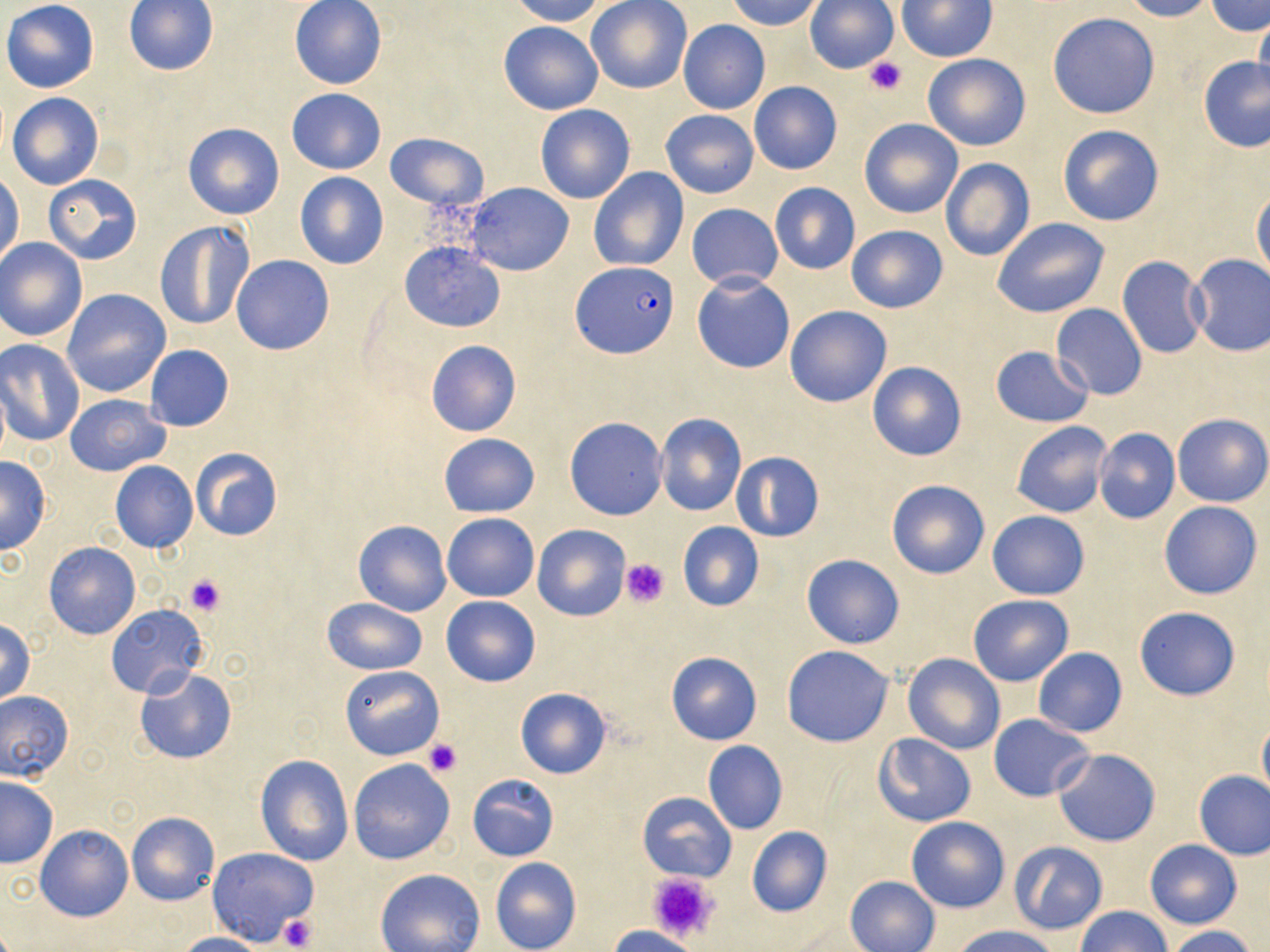

slide_level_diagnosis: Plasmodium falciparum
platelet_locations: 'approximate bounding boxes as (x1,y1)-(x2,y2) corner pairs in pixels: (863,55)-(908,97), (620,558)-(671,608), (184,573)-(227,616), (423,738)-(463,777), (645,871)-(722,947), (276,912)-(318,952)'
field_of_view: one of a larger specimen
preparation: thin blood smear
uninfected_red_blood_cell_locations: 'approximate bounding boxes as (x1,y1)-(x2,y2) corner pairs in pixels: (1,0)-(99,92), (289,0)-(386,89), (506,0)-(605,26), (727,0)-(827,32), (805,0)-(899,74), (1120,0)-(1216,21), (1207,0)-(1270,37), (123,1)-(219,75), (586,1)-(692,94), (897,1)-(996,61), (1047,13)-(1160,119), (1253,13)-(1270,102), (498,19)-(603,115), (678,19)-(770,114), (922,53)-(1031,151), (1197,55)-(1270,152), (749,81)-(842,175), (287,88)-(386,174), (7,92)-(103,190), (535,105)-(635,204), (661,110)-(759,198), (859,118)-(963,218), (183,122)-(284,219), (1057,125)-(1164,227), (384,132)-(486,211), (941,158)-(1034,261), (588,167)-(689,271), (1,169)-(23,268), (295,171)-(389,270), (43,174)-(142,264), (465,182)-(572,275), (770,183)-(860,274), (1251,190)-(1270,285), (687,203)-(782,290), (992,216)-(1111,318), (155,221)-(253,330), (845,225)-(949,312), (0,238)-(87,342), (399,242)-(506,332), (231,254)-(334,355), (1186,254)-(1270,357), (1116,256)-(1209,358), (692,274)-(794,373), (61,289)-(171,398), (1052,304)-(1147,399), (785,305)-(891,407), (0,340)-(85,446), (425,340)-(521,437), (144,344)-(235,432), (989,345)-(1095,427), (866,361)-(967,462), (0,374)-(9,469), (65,393)-(170,476), (655,412)-(747,516), (1174,414)-(1270,507), (565,418)-(667,521), (1011,421)-(1113,518), (1092,428)-(1181,525), (438,433)-(539,517), (189,447)-(284,541), (730,451)-(824,543), (0,454)-(51,556), (110,460)-(198,553), (887,479)-(992,579), (1158,501)-(1263,600), (986,511)-(1089,600), (442,514)-(539,601), (354,520)-(451,616), (676,521)-(765,612), (533,525)-(630,621), (44,543)-(140,640), (801,554)-(905,648), (968,593)-(1074,687), (440,594)-(542,686), (322,598)-(428,674), (105,605)-(207,699), (1135,607)-(1240,701), (1,619)-(37,706), (781,646)-(894,746), (1032,648)-(1127,738), (665,651)-(762,744), (902,652)-(1006,754), (340,666)-(444,760), (134,667)-(238,763), (514,686)-(612,780), (0,689)-(73,783), (987,714)-(1093,801), (1256,714)-(1270,809), (872,733)-(975,828), (702,741)-(787,835), (1052,747)-(1161,846), (255,754)-(354,867), (348,760)-(456,865), (1193,769)-(1269,860), (467,774)-(559,862), (0,776)-(58,867), (637,791)-(736,883), (127,812)-(218,905), (906,815)-(1009,913), (36,825)-(131,923), (746,826)-(833,918), (1144,839)-(1243,929), (1009,840)-(1108,934), (207,847)-(318,946), (490,857)-(582,952), (375,868)-(485,952), (845,875)-(940,952), (1075,906)-(1171,952), (952,925)-(1063,952), (1164,925)-(1260,952), (605,926)-(702,952), (175,932)-(265,951)'
plasmodium_falciparum_infected_red_blood_cell_locations: 'approximate bounding boxes as (x1,y1)-(x2,y2) corner pairs in pixels: (574,261)-(677,358)'
magnification: 1000x
stain: May-Grünwald-Giemsa
modality: optical microscopy
image_size: 1270×952 pixels